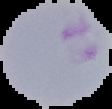
image type = segmented cell region on a black background
preparation = thin blood film
image size = 112×109 pixels
result = malaria parasites identified